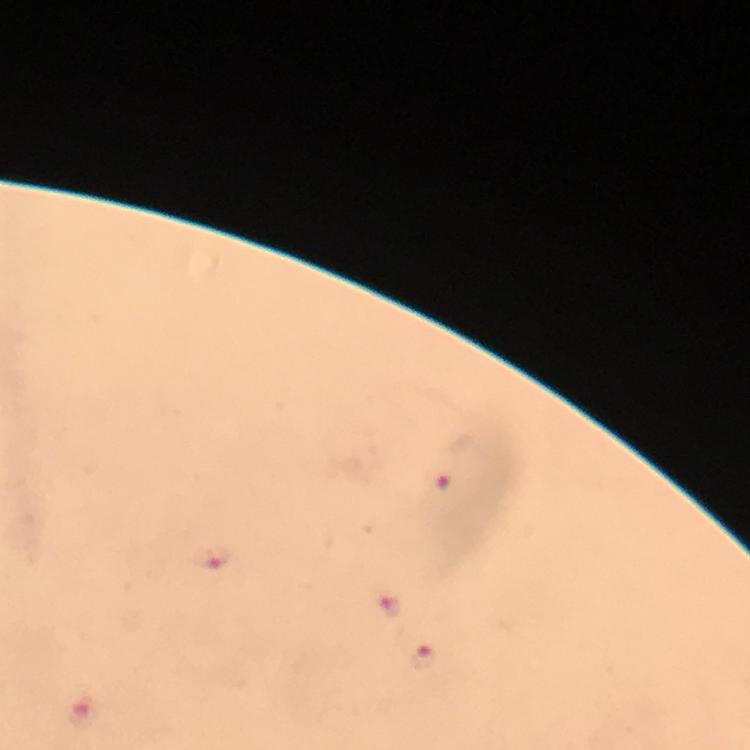 Approximate centers as {x, y} in pixels. Malaria parasite locations: {438, 478}, {214, 558}, {392, 603}, {424, 657}. Cropped region of a single field of view. Giemsa stain. At 100x magnification. From a malaria diagnostic workup. Image is 750×750 pixels. Thick blood smear. Smartphone photograph taken through a microscope. Immersion oil applied.